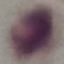

malaria_status: uninfected
preparation: thin blood smear
image_type: cell patch, automatically extracted from a larger field of view and resized to 64 × 64 pixels
stain: Giemsa
capture: smartphone through the microscope eyepiece